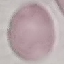

Summary:
  - Malaria status: uninfected
  - Image type: automatically extracted cell patch, resized to 64 × 64 pixels
  - Stain: Giemsa
  - Capture: smartphone through the microscope eyepiece
  - Preparation: thin blood film